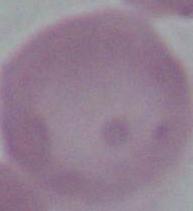

Summary:
  - Modality: photomicrograph
  - Magnification: 1000x
  - Identification: red blood cell